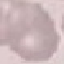
Result: no malaria parasites detected. Thin blood smear. Photographed with a smartphone camera at the microscope eyepiece. Cell patch, automatically extracted from a larger field of view and resized to 64 × 64 pixels. Giemsa-stained preparation.